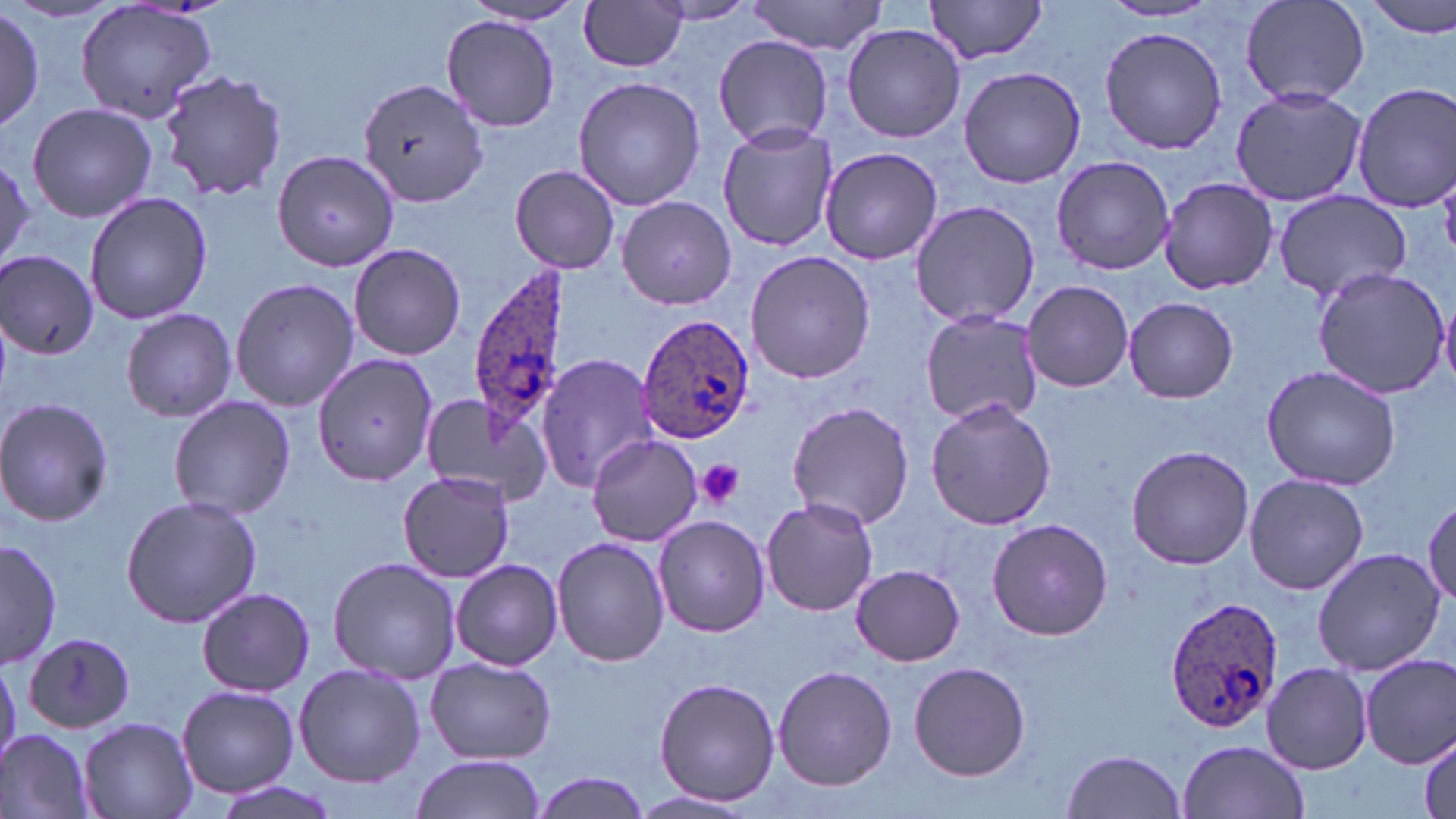

Approximate bounding boxes as (x1, y1, x2, y2) in pixels. Plasmodium ovale-infected red blood cell locations: (467, 264, 575, 447), (638, 314, 755, 445), (1164, 594, 1284, 733). Platelet locations: (695, 460, 746, 508). Uninfected red blood cell locations: (73, 0, 221, 125), (1365, 0, 1456, 39), (460, 1, 592, 29), (579, 1, 689, 73), (652, 1, 758, 25), (746, 1, 887, 54), (922, 1, 1051, 64), (1240, 1, 1370, 108), (1099, 2, 1223, 23), (1, 9, 44, 128), (442, 17, 560, 131), (842, 23, 965, 143), (1099, 24, 1227, 155), (713, 35, 837, 148), (957, 65, 1088, 188), (157, 70, 288, 203), (572, 75, 705, 212), (358, 78, 487, 210), (1352, 81, 1456, 212), (1230, 86, 1366, 207), (26, 102, 157, 224), (718, 123, 840, 252), (820, 145, 945, 265), (273, 149, 401, 275), (0, 153, 33, 270), (1050, 154, 1175, 276), (509, 163, 622, 275), (1155, 177, 1279, 294), (1271, 189, 1411, 304), (83, 192, 214, 324), (616, 195, 736, 309), (909, 198, 1040, 329), (349, 242, 466, 360), (746, 251, 875, 384), (1, 252, 100, 358), (1311, 266, 1449, 397), (230, 277, 360, 412), (1022, 281, 1134, 391), (1124, 296, 1238, 403), (121, 308, 236, 422), (919, 308, 1043, 428), (311, 352, 438, 486), (537, 352, 660, 491), (1261, 364, 1401, 491), (417, 391, 552, 509), (168, 396, 296, 521), (0, 397, 115, 528), (924, 399, 1057, 532), (786, 401, 915, 530), (586, 434, 703, 548), (1125, 444, 1255, 570), (398, 469, 516, 582), (1243, 472, 1369, 596), (122, 495, 262, 627), (1425, 495, 1456, 606), (761, 497, 878, 616), (653, 515, 770, 638), (987, 517, 1112, 640), (552, 536, 669, 667), (1, 538, 60, 670), (1311, 547, 1444, 676), (327, 556, 460, 683), (452, 558, 562, 672), (852, 564, 964, 666), (196, 586, 315, 697), (23, 634, 137, 732), (1362, 655, 1455, 770), (426, 656, 556, 764), (0, 660, 21, 766), (909, 661, 1031, 781), (293, 662, 425, 787), (1261, 663, 1373, 774), (773, 664, 897, 790), (653, 676, 781, 806), (176, 686, 300, 799), (78, 716, 198, 819), (1415, 728, 1456, 819), (0, 729, 94, 819), (1177, 740, 1310, 819), (1061, 749, 1188, 819), (409, 754, 548, 819), (531, 771, 654, 818), (205, 777, 342, 819), (630, 790, 758, 816). Slide-level diagnosis: Plasmodium ovale. Image is 1456×819 pixels. May-Grünwald-Giemsa stain. Light microscopy. Single field of view. Thin blood film. 1000x magnification.